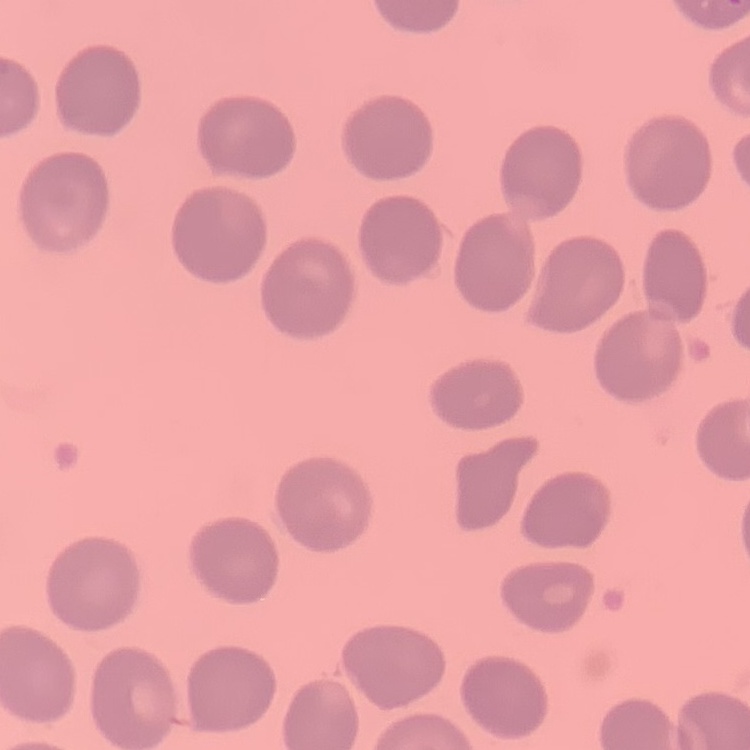

erythrocyte morphology = no rouleaux formation
image type = square crop of a larger photomicrograph
preparation = thin blood smear
stain = Field's or Giemsa